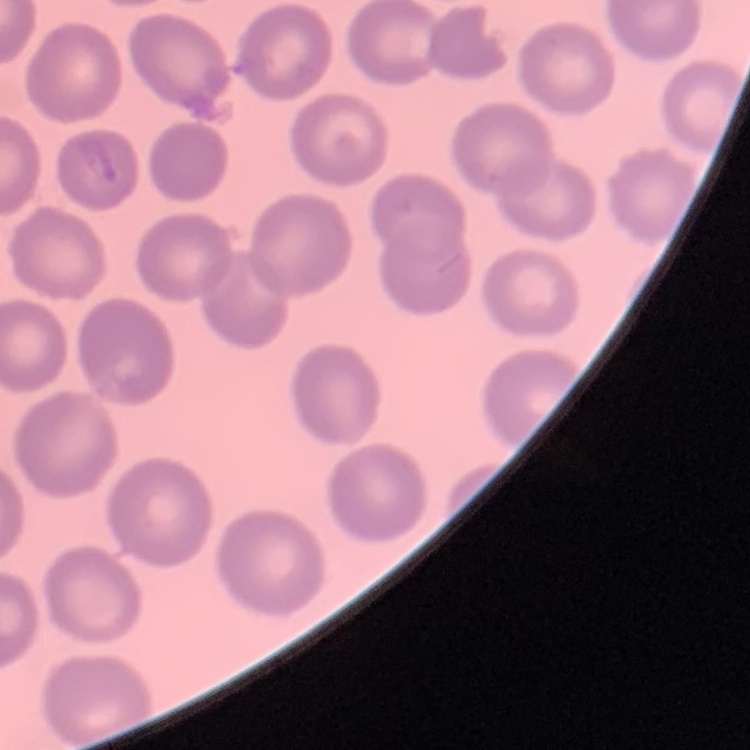
{
  "erythrocyte_morphology": "no rouleaux formation",
  "preparation": "thin blood smear",
  "image_type": "one tile cut from a larger photomicrograph",
  "stain": "Field's or Giemsa"
}